Classify this cell by malaria status.
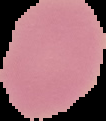
It is uninfected.

{
  "image_size": "106×121 pixels",
  "image_type": "cell region segmented out of the field of view; surrounding area masked to black",
  "preparation": "thin blood smear"
}